Report the malaria status.
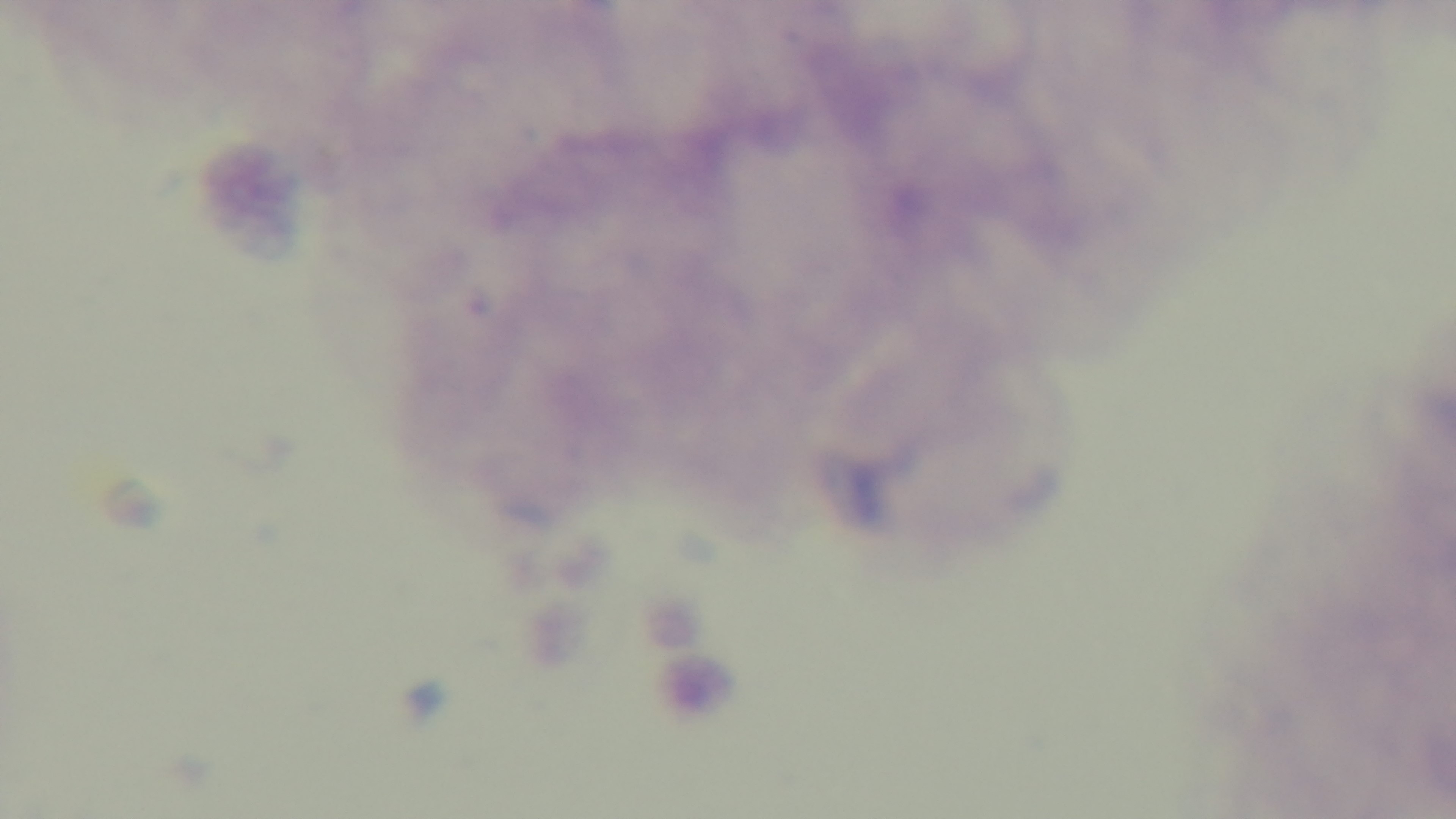

Uninfected.

Summary:
  - Preparation: thick blood film
  - Stain: Giemsa
  - Modality: light microscopy
  - Objective: 100x oil immersion
  - Field of view: single
  - Capture: mounted 4K digital camera